Locate the cells, classifying each as a parasitized RBC, an uninfected RBC, or a WBC.
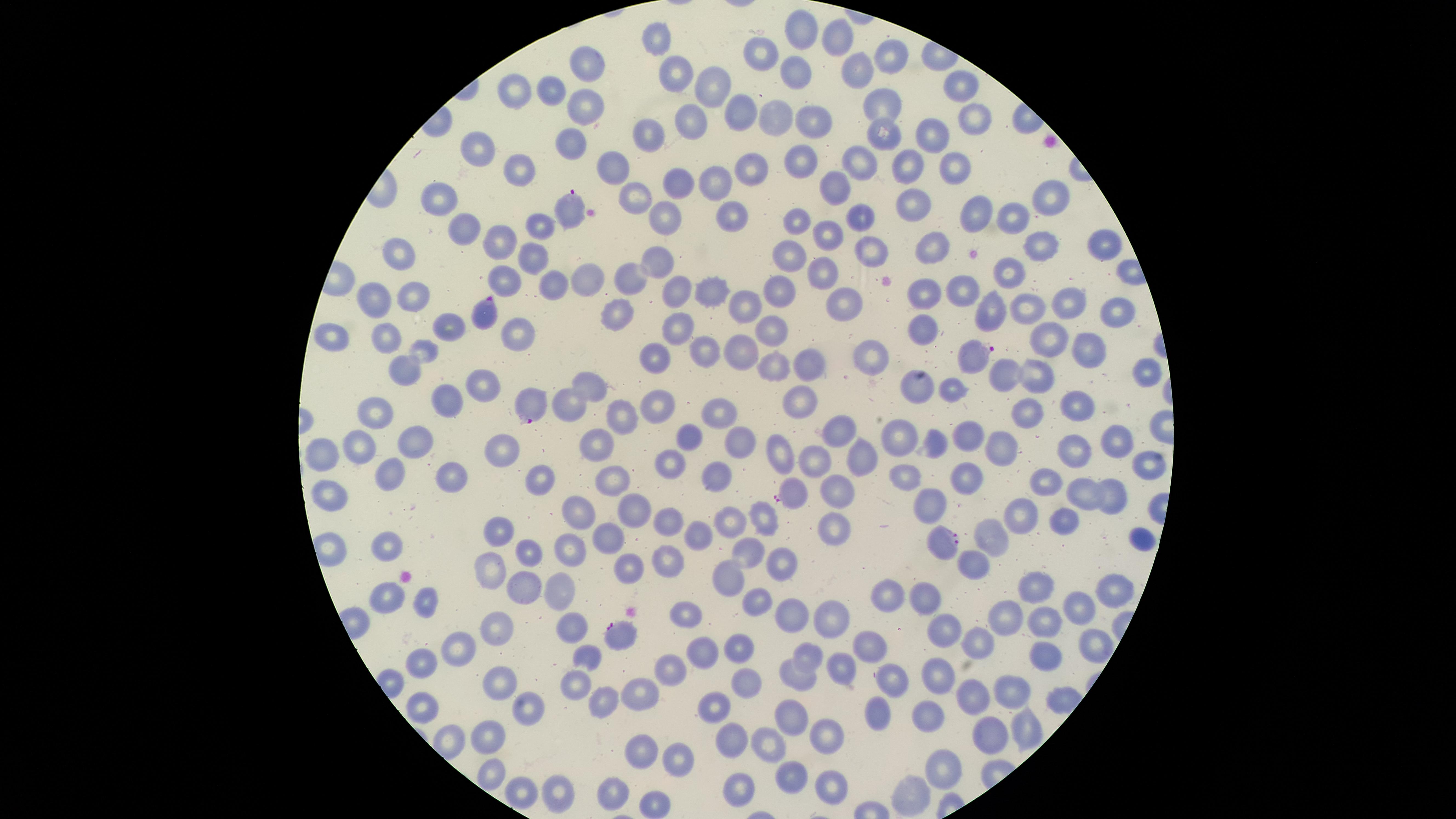
Approximate marker points as [x, y] in pixels.
Parasitized RBCs: [571, 211], [485, 315], [970, 355], [531, 405], [788, 491], [947, 545], [619, 634].
Uninfected RBCs: [800, 34], [656, 40], [838, 40], [891, 51], [759, 57], [796, 66], [585, 69], [860, 71], [672, 74], [715, 80], [960, 87], [511, 89], [547, 93], [579, 104], [884, 104], [737, 108], [771, 118], [692, 120], [974, 121], [811, 122], [646, 132], [929, 132], [883, 134], [570, 143], [477, 153], [798, 156], [860, 161], [953, 165], [907, 167], [747, 169], [610, 170], [518, 171], [712, 179], [683, 187], [830, 189], [1044, 198], [634, 200], [432, 204], [907, 207], [969, 212], [728, 213], [862, 213], [1011, 218], [801, 219], [533, 220], [657, 222], [466, 232], [825, 232], [497, 243], [1043, 243], [1098, 244], [931, 247], [529, 250], [874, 251], [401, 256], [792, 259], [652, 261], [1007, 272], [626, 274], [824, 274], [581, 276], [547, 281], [675, 288], [923, 291], [964, 291], [709, 292], [777, 295], [377, 296], [412, 297], [1065, 304], [841, 306], [1029, 308], [1113, 309], [746, 310], [991, 310], [617, 312], [448, 326], [672, 329], [925, 329], [771, 330], [512, 332], [386, 338], [1047, 338], [332, 342], [707, 347], [425, 351], [1089, 352], [742, 356], [868, 361], [652, 363], [810, 366], [774, 369], [1005, 373], [394, 374], [1032, 374], [1148, 374], [916, 382], [486, 386], [950, 386], [590, 387], [443, 401], [656, 401], [798, 401], [1075, 402], [571, 409], [718, 411], [380, 412], [630, 414], [1025, 416], [835, 432], [899, 432], [689, 433], [964, 437], [1113, 440], [417, 441], [595, 442], [736, 442], [995, 442], [773, 444], [933, 444], [1073, 445], [354, 447], [508, 448], [858, 459], [326, 463], [669, 463], [1144, 464], [817, 468], [402, 473], [447, 476], [717, 477], [605, 478], [903, 480], [968, 481], [541, 482], [1048, 486], [837, 493], [1083, 493], [329, 494], [1114, 501], [934, 502], [629, 506], [578, 508], [1019, 509], [730, 516], [760, 516], [668, 518], [1058, 522], [835, 524], [498, 531], [993, 538], [1140, 538], [694, 539], [608, 541], [382, 549], [323, 550], [564, 551], [526, 552], [748, 554], [669, 560], [787, 562], [974, 563], [626, 565], [488, 568], [724, 577], [523, 584], [1038, 585], [558, 592], [922, 593], [1104, 593], [386, 595], [424, 596], [887, 600], [751, 605], [1077, 608], [791, 611], [1005, 612], [684, 617], [824, 618], [1046, 621], [493, 624], [570, 627], [941, 627], [867, 642], [975, 642], [1095, 646], [733, 647], [466, 649], [809, 654], [700, 656], [1037, 656], [587, 657], [425, 662], [675, 669], [834, 669], [797, 672], [941, 673], [891, 676], [576, 677], [742, 677], [501, 682], [970, 687], [1012, 692], [640, 693], [603, 698], [419, 707], [716, 708], [928, 709], [878, 710], [528, 715], [788, 719], [1027, 730], [989, 734], [735, 736], [825, 737], [490, 738], [769, 740], [641, 748], [677, 763], [943, 769], [493, 777], [791, 781], [518, 789], [732, 789], [830, 790], [610, 792], [554, 794], [907, 794], [656, 801].
No WBCs identified.

Summary:
  - Visible region: circular
  - Capture: smartphone photograph through the microscope eyepiece
  - Field of view: single
  - Species: Plasmodium falciparum
  - Stain: Giemsa
  - Preparation: thin blood smear
  - Image size: 1456×819 pixels